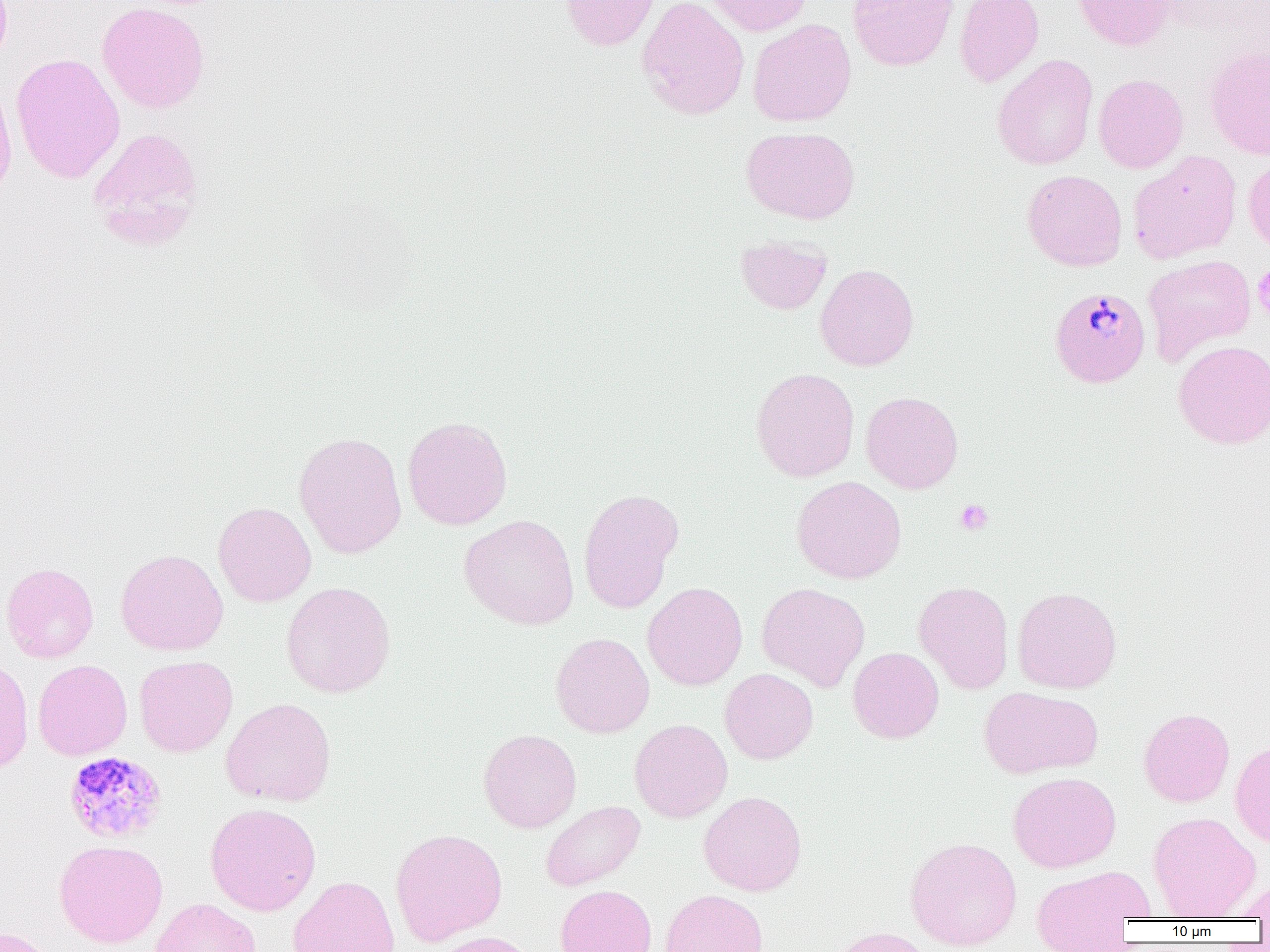

Approximate bounding boxes as named x1/y1/x2/y2 corners in pixels. Platelet locations: (x1=1253, y1=264, x2=1270, y2=322), (x1=955, y1=499, x2=993, y2=535). Plasmodium malariae-infected red blood cell locations: (x1=1049, y1=287, x2=1150, y2=388), (x1=64, y1=751, x2=168, y2=843). Uninfected red blood cell locations: (x1=559, y1=0, x2=660, y2=51), (x1=637, y1=0, x2=750, y2=121), (x1=702, y1=0, x2=813, y2=36), (x1=848, y1=0, x2=959, y2=71), (x1=954, y1=0, x2=1044, y2=88), (x1=1073, y1=0, x2=1176, y2=50), (x1=97, y1=2, x2=210, y2=114), (x1=748, y1=19, x2=856, y2=127), (x1=1203, y1=43, x2=1270, y2=159), (x1=10, y1=53, x2=125, y2=184), (x1=992, y1=54, x2=1098, y2=170), (x1=1094, y1=74, x2=1189, y2=173), (x1=0, y1=76, x2=17, y2=203), (x1=88, y1=126, x2=205, y2=248), (x1=741, y1=126, x2=860, y2=224), (x1=1128, y1=151, x2=1242, y2=263), (x1=1243, y1=154, x2=1270, y2=255), (x1=1022, y1=170, x2=1127, y2=271), (x1=736, y1=235, x2=832, y2=314), (x1=1143, y1=254, x2=1256, y2=364), (x1=814, y1=263, x2=919, y2=371), (x1=1173, y1=340, x2=1270, y2=449), (x1=751, y1=367, x2=860, y2=482), (x1=861, y1=391, x2=964, y2=494), (x1=402, y1=416, x2=513, y2=531), (x1=293, y1=431, x2=407, y2=559), (x1=792, y1=476, x2=907, y2=583), (x1=577, y1=488, x2=684, y2=614), (x1=213, y1=502, x2=317, y2=607), (x1=459, y1=514, x2=580, y2=630), (x1=116, y1=549, x2=229, y2=656), (x1=1, y1=562, x2=99, y2=663), (x1=913, y1=580, x2=1014, y2=694), (x1=281, y1=581, x2=396, y2=698), (x1=642, y1=582, x2=748, y2=691), (x1=756, y1=582, x2=870, y2=692), (x1=1013, y1=586, x2=1122, y2=693), (x1=550, y1=632, x2=655, y2=737), (x1=848, y1=647, x2=944, y2=743), (x1=134, y1=655, x2=238, y2=757), (x1=0, y1=656, x2=34, y2=774), (x1=33, y1=659, x2=132, y2=760), (x1=720, y1=668, x2=818, y2=764), (x1=979, y1=686, x2=1102, y2=779), (x1=220, y1=698, x2=336, y2=807), (x1=1138, y1=708, x2=1235, y2=807), (x1=629, y1=719, x2=733, y2=823), (x1=478, y1=728, x2=582, y2=833), (x1=1230, y1=740, x2=1270, y2=847), (x1=1007, y1=771, x2=1121, y2=873), (x1=698, y1=790, x2=807, y2=896), (x1=540, y1=800, x2=646, y2=891), (x1=205, y1=803, x2=321, y2=916), (x1=1148, y1=812, x2=1260, y2=919), (x1=390, y1=828, x2=507, y2=947), (x1=905, y1=837, x2=1022, y2=951), (x1=54, y1=839, x2=168, y2=949), (x1=1030, y1=866, x2=1153, y2=951), (x1=287, y1=876, x2=401, y2=952), (x1=1233, y1=879, x2=1270, y2=921), (x1=555, y1=884, x2=657, y2=952), (x1=660, y1=889, x2=768, y2=952), (x1=150, y1=898, x2=261, y2=952), (x1=826, y1=926, x2=937, y2=952), (x1=1, y1=927, x2=62, y2=952), (x1=428, y1=931, x2=540, y2=952). Slide-level diagnosis: Plasmodium malariae. Optical microscopy. Thin blood smear. Image is 1270×952 pixels. Single field of view. Captured at 1000x magnification.